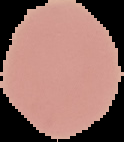
image type = segmented cell region on a black background
image size = 124×142 pixels
preparation = thin blood smear
malaria status = uninfected